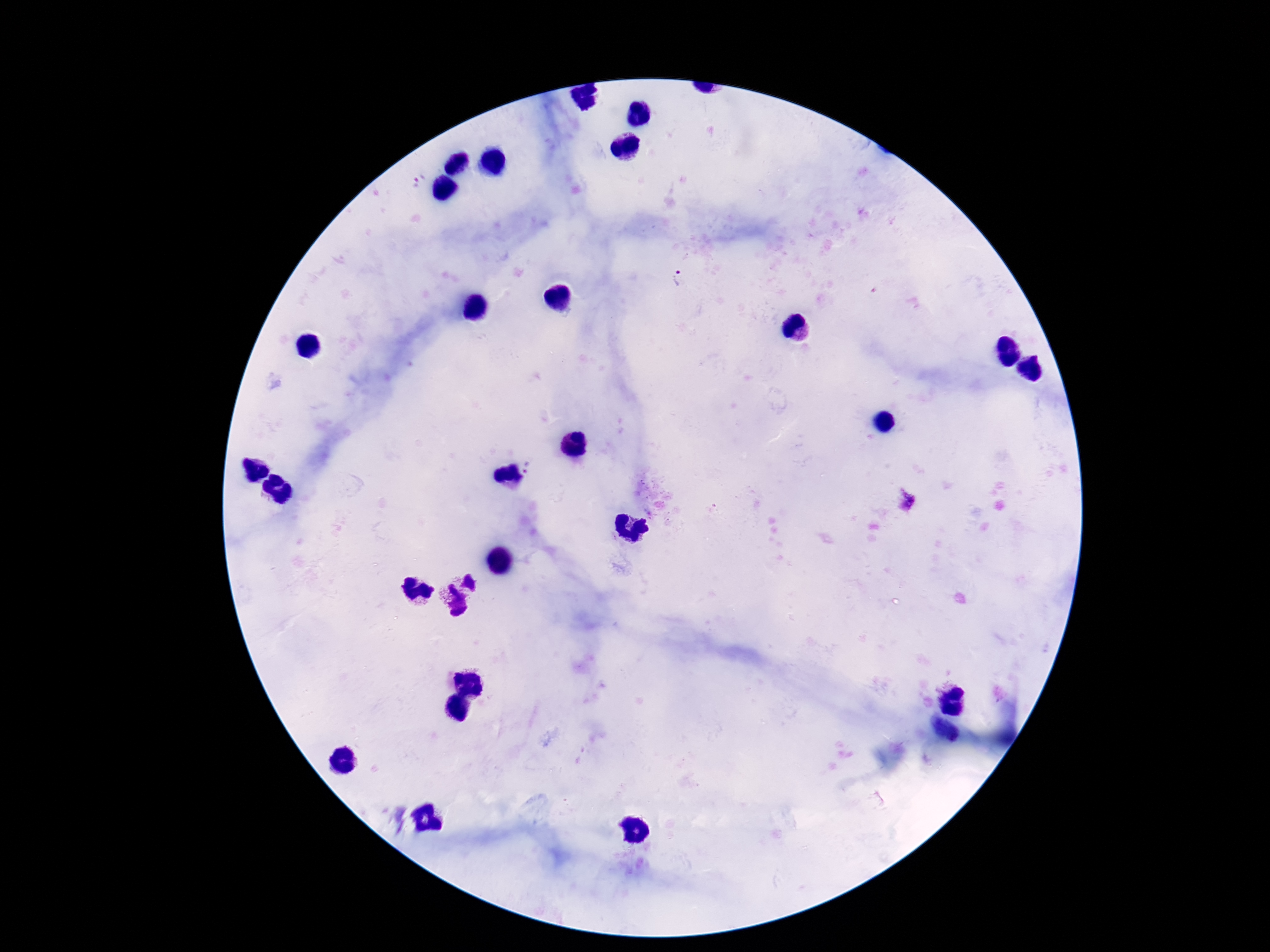
Approximate object centers, in pixels from the top-left corner.
Summary:
  - Plasmodium parasite locations: (x=683, y=282), (x=531, y=469)
  - Capture: smartphone camera through the microscope eyepiece
  - Magnification: 100x
  - Stain: Giemsa
  - Preparation: thick peripheral-blood smear
  - Patient malaria status: infected
  - Image size: 1270×952 pixels
  - Field of view: one from this slide